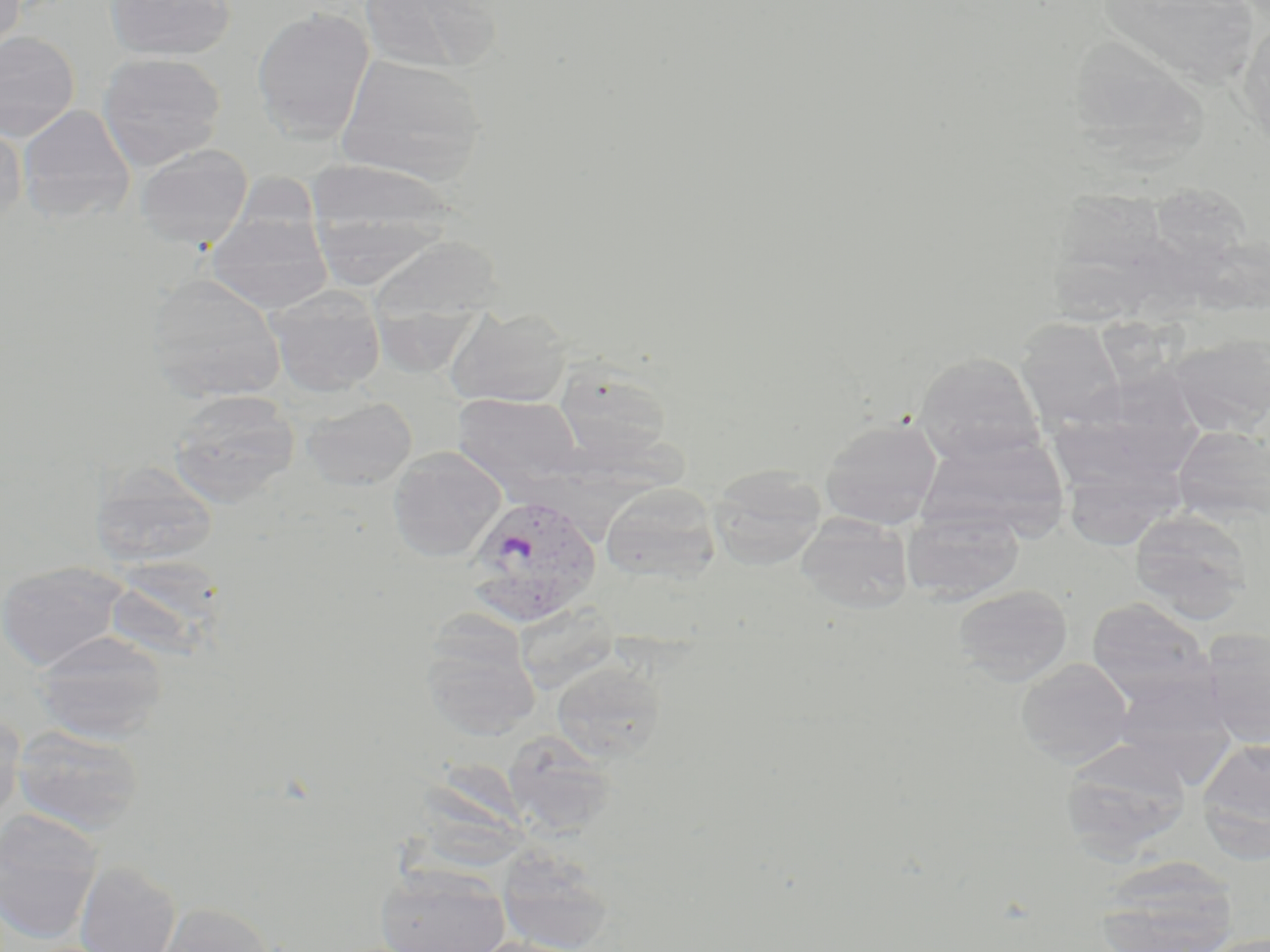 Approximate bounding boxes as [x1, y1, x2, y2] in pixels. Uninfected red blood cell locations: [0, 0, 25, 54], [105, 0, 236, 61], [360, 0, 500, 74], [1095, 0, 1266, 91], [252, 7, 374, 143], [1236, 16, 1270, 149], [0, 31, 80, 140], [1077, 45, 1211, 178], [97, 52, 227, 169], [335, 53, 487, 186], [17, 104, 136, 225], [0, 122, 27, 226], [135, 144, 253, 249], [304, 158, 457, 282], [1149, 183, 1254, 269], [207, 211, 333, 314], [367, 236, 504, 326], [145, 273, 286, 403], [267, 285, 386, 398], [447, 306, 573, 407], [1015, 319, 1126, 430], [1167, 334, 1270, 435], [913, 352, 1046, 467], [552, 362, 676, 466], [166, 389, 300, 506], [453, 392, 583, 491], [300, 395, 417, 491], [820, 416, 942, 530], [1172, 425, 1270, 526], [916, 432, 1067, 540], [387, 446, 506, 562], [1059, 461, 1185, 550], [90, 462, 219, 567], [708, 464, 826, 570], [601, 482, 721, 586], [902, 507, 1025, 603], [1129, 509, 1255, 623], [794, 513, 913, 613], [0, 561, 130, 670], [952, 584, 1073, 686], [1086, 597, 1214, 706], [420, 617, 541, 742], [1199, 629, 1270, 746], [32, 630, 170, 743], [1016, 658, 1135, 767], [551, 661, 666, 762], [0, 710, 25, 826], [11, 724, 146, 835], [502, 729, 617, 835], [1197, 736, 1270, 856], [1060, 740, 1192, 858], [432, 755, 532, 868], [0, 808, 104, 944], [497, 848, 615, 952], [1095, 857, 1239, 952], [74, 860, 181, 952], [373, 866, 511, 952], [151, 901, 277, 952], [464, 937, 591, 952]. Plasmodium vivax-infected red blood cell locations: [466, 493, 602, 625]. Slide-level diagnosis: Plasmodium vivax. Image is 1270×952 pixels. Captured at 1000x magnification. May-Grünwald-Giemsa stain. One field of a larger specimen. Light microscopy. Thin blood smear.